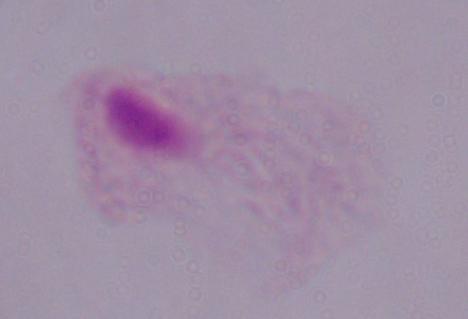

identification: trichomonad
magnification: 1000x
modality: photomicrograph